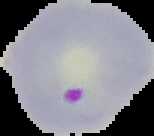
Summary:
  - Preparation: thin blood smear
  - Malaria status: parasitized
  - Image type: segmented cell region on a black background
  - Image size: 154×136 pixels